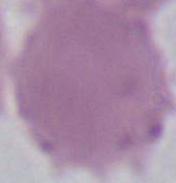
A red blood cell is shown. Micrograph. 1000x magnification.